Classify this cell by malaria status.
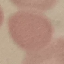
It is uninfected.

Summary:
  - Capture: smartphone through the microscope eyepiece
  - Stain: Giemsa
  - Image type: automatically extracted cell patch, resized to 64 × 64 pixels
  - Preparation: thin blood film